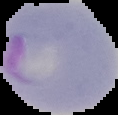

Result: Plasmodium parasites detected. Segmented cell region on a black background. From a thin blood film. Image is 118×115 pixels.